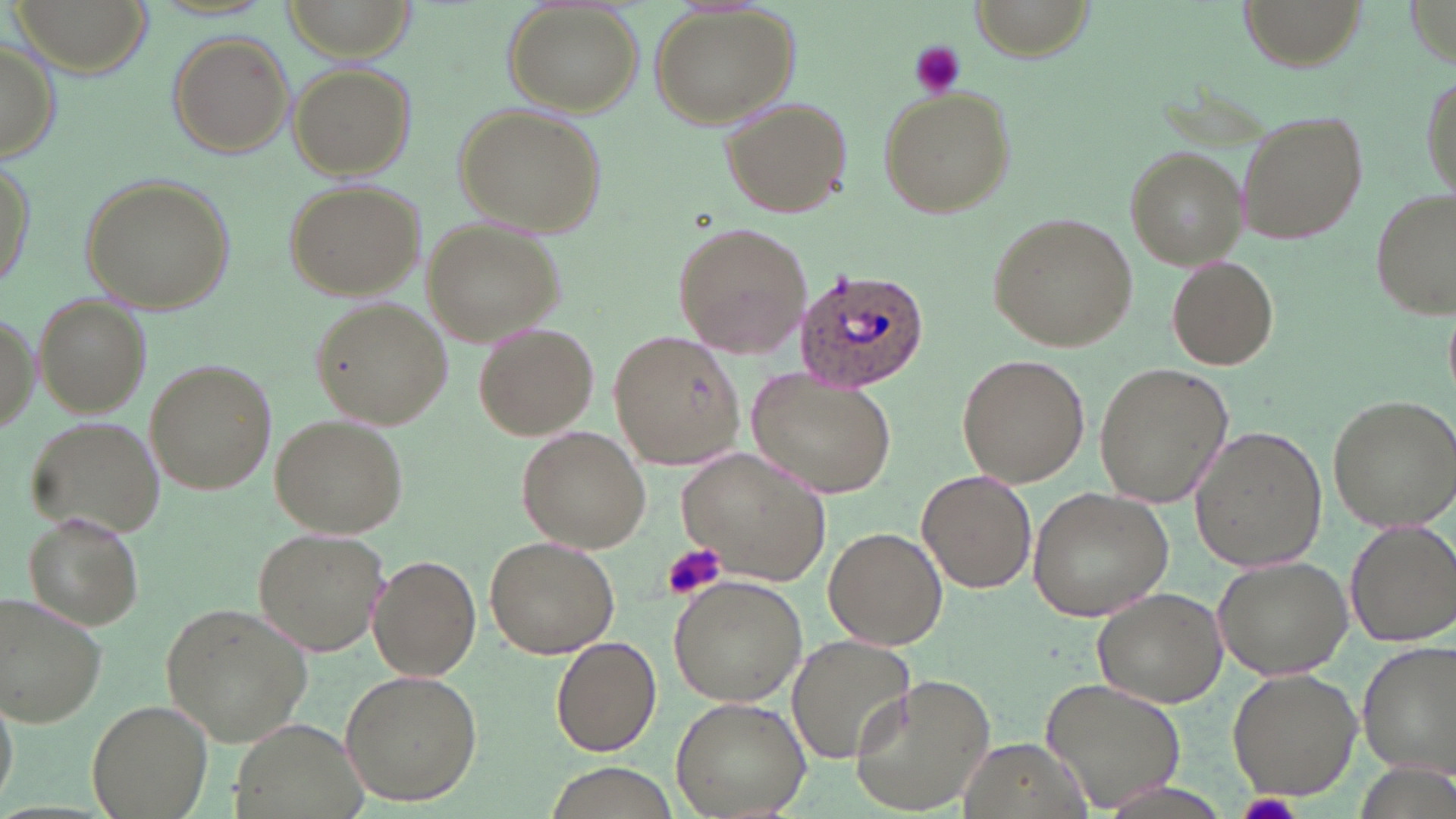
slide-level diagnosis = Plasmodium ovale
uninfected red blood cell locations = approximate bounding boxes as named x1/y1/x2/y2 corners in pixels: (x1=8, y1=0, x2=154, y2=78), (x1=285, y1=0, x2=412, y2=58), (x1=1237, y1=0, x2=1368, y2=68), (x1=647, y1=4, x2=800, y2=130), (x1=506, y1=5, x2=641, y2=115), (x1=165, y1=30, x2=294, y2=159), (x1=0, y1=33, x2=60, y2=164), (x1=290, y1=62, x2=415, y2=181), (x1=1417, y1=65, x2=1454, y2=206), (x1=877, y1=86, x2=1017, y2=218), (x1=720, y1=96, x2=853, y2=218), (x1=454, y1=102, x2=605, y2=240), (x1=1235, y1=106, x2=1372, y2=246), (x1=1124, y1=146, x2=1246, y2=268), (x1=1, y1=153, x2=36, y2=300), (x1=77, y1=171, x2=233, y2=313), (x1=284, y1=179, x2=424, y2=301), (x1=1369, y1=188, x2=1454, y2=321), (x1=988, y1=212, x2=1137, y2=351), (x1=423, y1=221, x2=561, y2=344), (x1=671, y1=221, x2=811, y2=359), (x1=1167, y1=256, x2=1280, y2=370), (x1=34, y1=292, x2=153, y2=417), (x1=312, y1=297, x2=451, y2=428), (x1=0, y1=307, x2=40, y2=442), (x1=475, y1=322, x2=597, y2=440), (x1=608, y1=333, x2=745, y2=469), (x1=957, y1=353, x2=1090, y2=486), (x1=145, y1=358, x2=275, y2=495), (x1=1094, y1=362, x2=1233, y2=510), (x1=747, y1=371, x2=897, y2=498), (x1=1326, y1=394, x2=1456, y2=533), (x1=271, y1=412, x2=410, y2=537), (x1=26, y1=415, x2=163, y2=537), (x1=518, y1=426, x2=654, y2=553), (x1=1192, y1=427, x2=1328, y2=572), (x1=679, y1=447, x2=830, y2=582), (x1=917, y1=469, x2=1036, y2=594), (x1=1028, y1=487, x2=1177, y2=620), (x1=22, y1=510, x2=145, y2=632), (x1=1343, y1=519, x2=1456, y2=649), (x1=823, y1=526, x2=948, y2=649), (x1=252, y1=527, x2=389, y2=657), (x1=485, y1=533, x2=621, y2=658), (x1=1213, y1=552, x2=1354, y2=681), (x1=370, y1=555, x2=481, y2=681), (x1=670, y1=573, x2=809, y2=705), (x1=1090, y1=587, x2=1228, y2=709), (x1=0, y1=593, x2=107, y2=730), (x1=157, y1=601, x2=313, y2=747), (x1=552, y1=635, x2=662, y2=756), (x1=786, y1=636, x2=915, y2=766), (x1=1355, y1=643, x2=1456, y2=779), (x1=339, y1=668, x2=482, y2=806), (x1=1227, y1=668, x2=1360, y2=800), (x1=847, y1=674, x2=998, y2=815), (x1=1042, y1=677, x2=1187, y2=813), (x1=672, y1=695, x2=813, y2=819), (x1=87, y1=698, x2=216, y2=819), (x1=226, y1=716, x2=374, y2=819), (x1=959, y1=739, x2=1101, y2=818), (x1=538, y1=763, x2=687, y2=818)
Plasmodium ovale-infected red blood cell locations = approximate bounding boxes as named x1/y1/x2/y2 corners in pixels: (x1=793, y1=265, x2=934, y2=392)
field of view = single
image size = 1456×819 pixels
modality = light microscopy
platelet locations = approximate bounding boxes as named x1/y1/x2/y2 corners in pixels: (x1=906, y1=41, x2=966, y2=99), (x1=661, y1=541, x2=728, y2=600)
stain = May-Grünwald-Giemsa
magnification = 1000x
preparation = thin blood film